Point out each Plasmodium parasite.
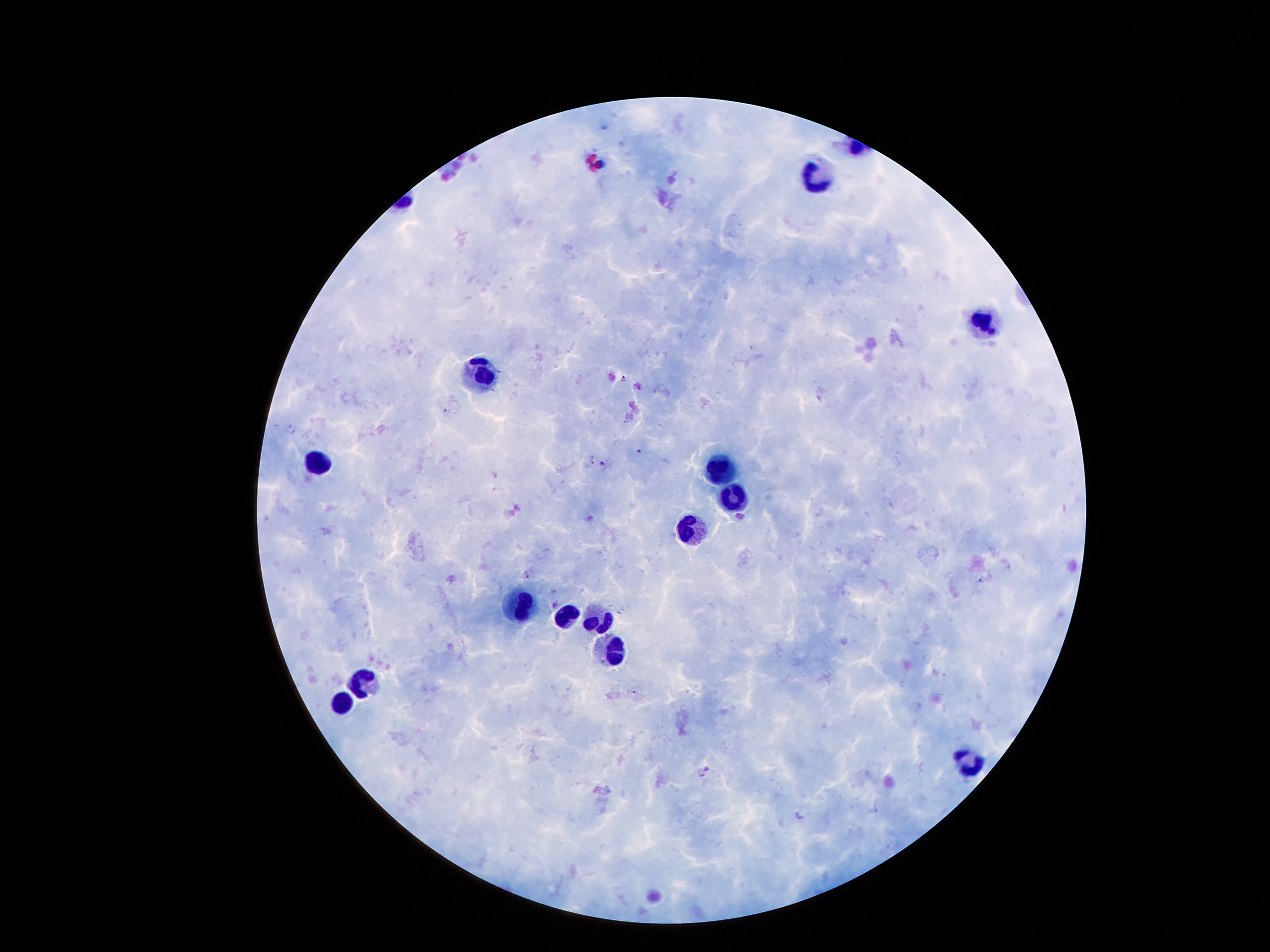

Approximate centers as (x, y) in pixels.
Plasmodium parasites: (624, 378), (638, 452), (589, 459), (602, 464), (527, 574), (633, 691), (708, 768), (701, 773).

Summary:
  - Leukocyte locations: (817, 176), (984, 323), (482, 372), (317, 461), (721, 470), (733, 497), (692, 530), (521, 607), (565, 618), (598, 618), (607, 652), (360, 679), (342, 702), (968, 761)
  - Image size: 1270×952 pixels
  - Preparation: thick peripheral-blood smear
  - Patient malaria status: positive for Plasmodium falciparum
  - Field of view: one from this slide
  - Stain: Giemsa
  - Capture: smartphone camera through the microscope eyepiece
  - Magnification: 100x